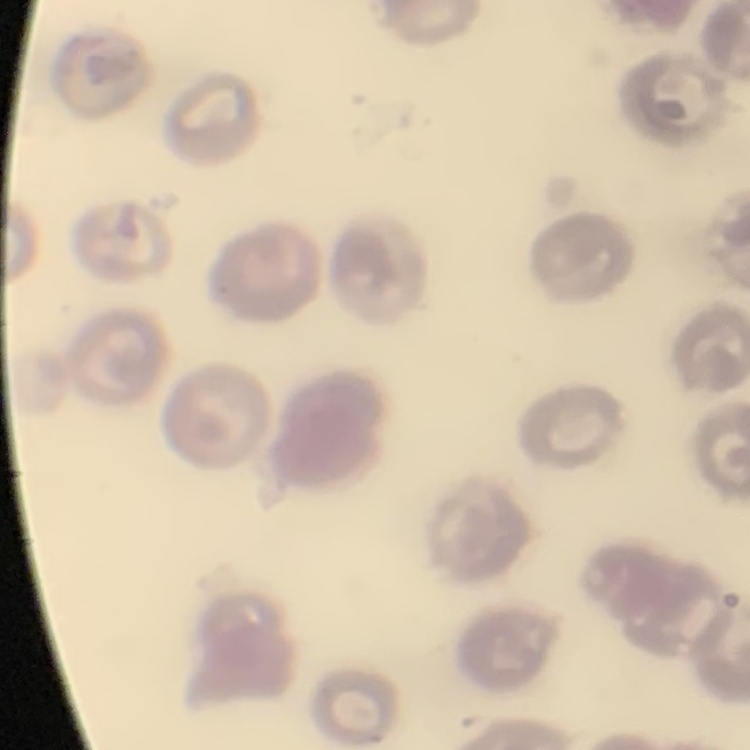
Summary:
  - Red blood cell morphology: no rouleaux formation
  - Stain: Field's or Giemsa
  - Image type: one tile cut from a larger photomicrograph
  - Preparation: thin blood film